Locate every malaria parasite.
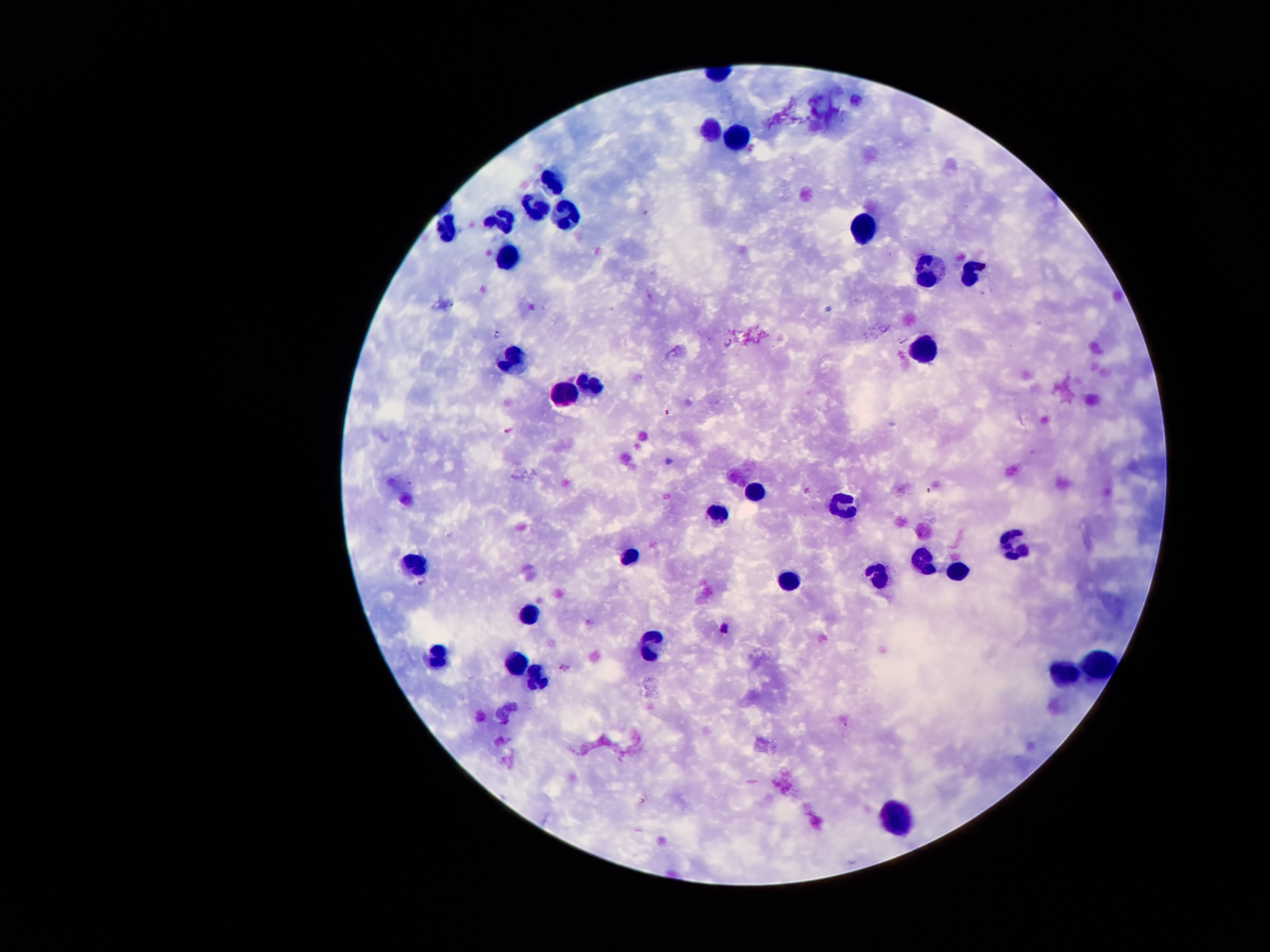
Approximate centers as [x, y] in pixels.
Malaria parasites: [499, 333], [904, 340], [728, 343], [667, 413], [670, 461], [423, 582], [590, 623], [725, 627], [565, 669].

leukocyte locations = [709, 129], [738, 134], [552, 183], [535, 208], [564, 217], [501, 223], [864, 228], [446, 230], [508, 257], [930, 269], [968, 274], [922, 346], [516, 363], [589, 383], [565, 394], [753, 490], [844, 504], [719, 512], [1011, 543], [631, 555], [919, 555], [416, 560], [952, 574], [789, 576], [875, 576], [530, 610], [652, 648], [437, 653], [517, 660], [1096, 662], [1063, 674], [535, 677], [893, 814]
magnification = 100x
patient malaria status = positive for Plasmodium falciparum
image size = 1270×952 pixels
field of view = one from this slide
preparation = thick blood film
stain = Giemsa
capture = smartphone camera through the microscope eyepiece